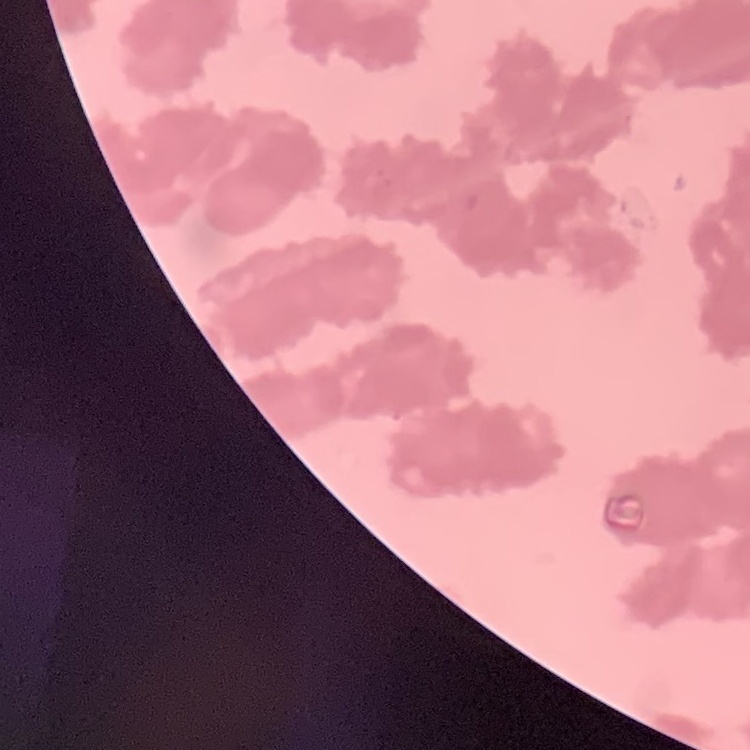
erythrocyte_morphology: rouleaux formation
preparation: thin peripheral smear
image_type: one tile cut from a larger photomicrograph
stain: Field's or Giemsa